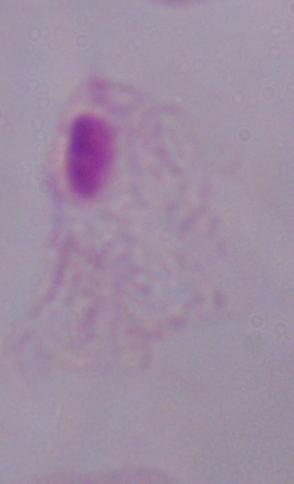
magnification = 1000x
modality = photomicrograph
identification = trichomonad